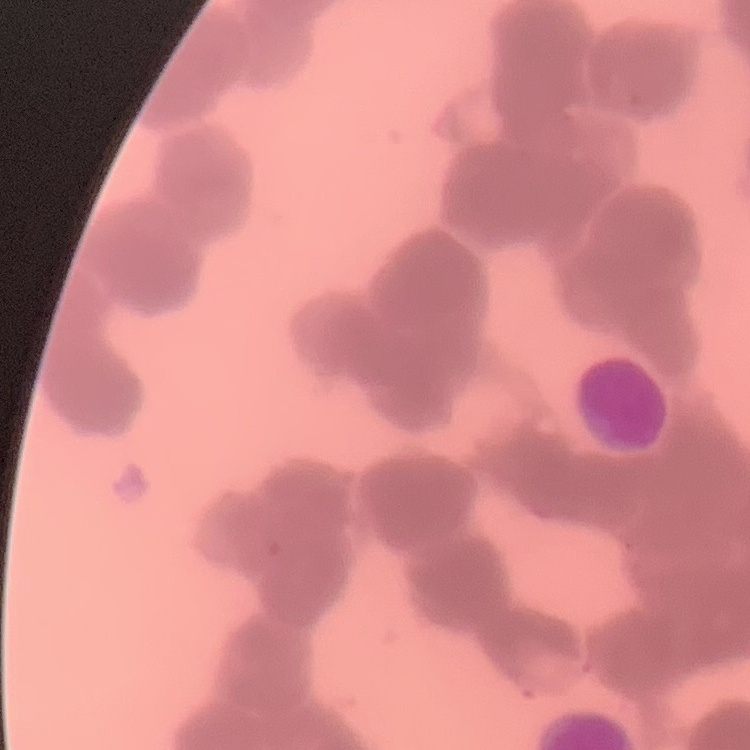

Summary:
  - Red blood cell morphology: rouleaux formation
  - Stain: Field's or Giemsa
  - Image type: square crop of a larger photomicrograph
  - Preparation: thin blood film